Classify this cell by malaria status.
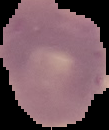
It is parasitized.

Image is 109×130 pixels. Cell region segmented out of the field of view; the surrounding area is masked to black. From a thin blood smear.